State which cell type is depicted.
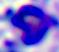

A leukocyte.

Summary:
  - Modality: micrograph
  - Magnification: 400x